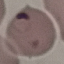
Summary:
  - Malaria status: parasitized
  - Stain: Giemsa
  - Preparation: thin blood film
  - Capture: smartphone through the microscope eyepiece
  - Image type: cell patch, automatically extracted from a larger field of view and resized to 64 × 64 pixels